Describe the morphology of the red blood cells.
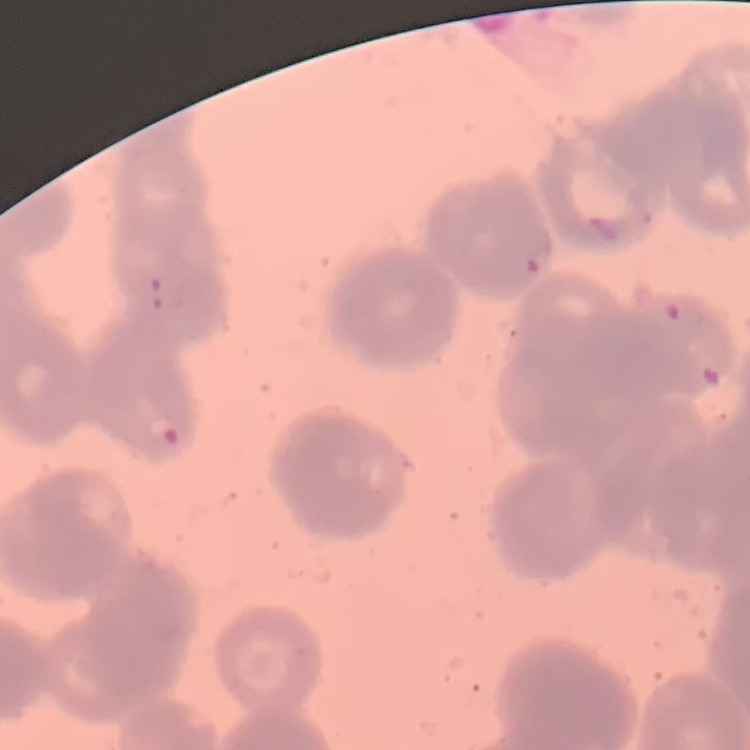

Rouleaux formation.

Thin blood film. Field's or Giemsa stain. One tile cut from a larger photomicrograph.